Identify the malaria species.
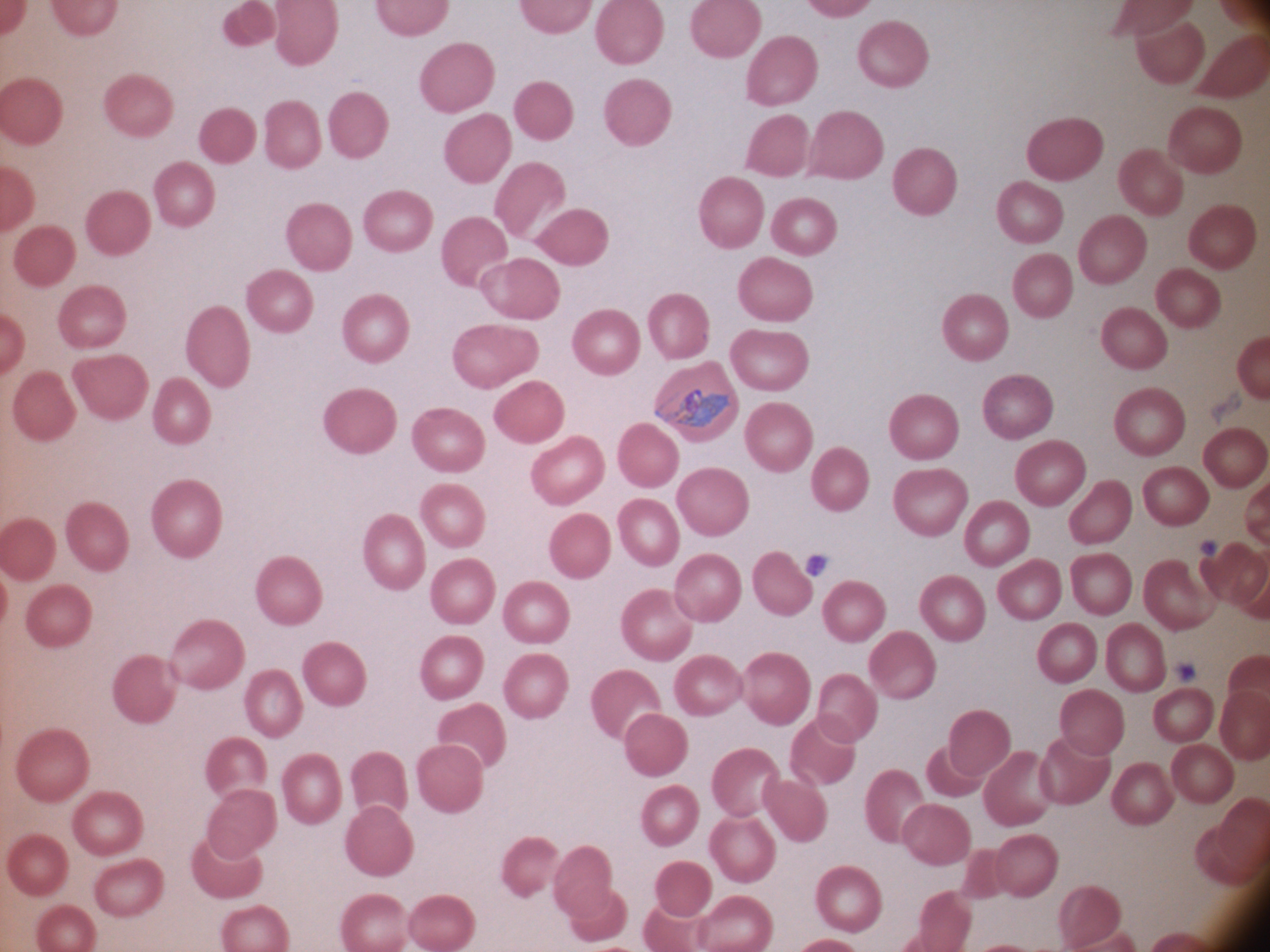
Plasmodium ovale.

Approximate bounding boxes as (x1, y1, x2, y2) in pixels, from the source annotation, which is not necessarily exhaustive.
Summary:
  - Trophozoite locations: (655, 389, 732, 427)
  - Microscope: Leica DM2000 with built-in camera
  - Image size: 1270×952 pixels
  - Field of view: one from this slide
  - Magnification: 100x
  - Stain: Giemsa
  - Preparation: thin blood smear